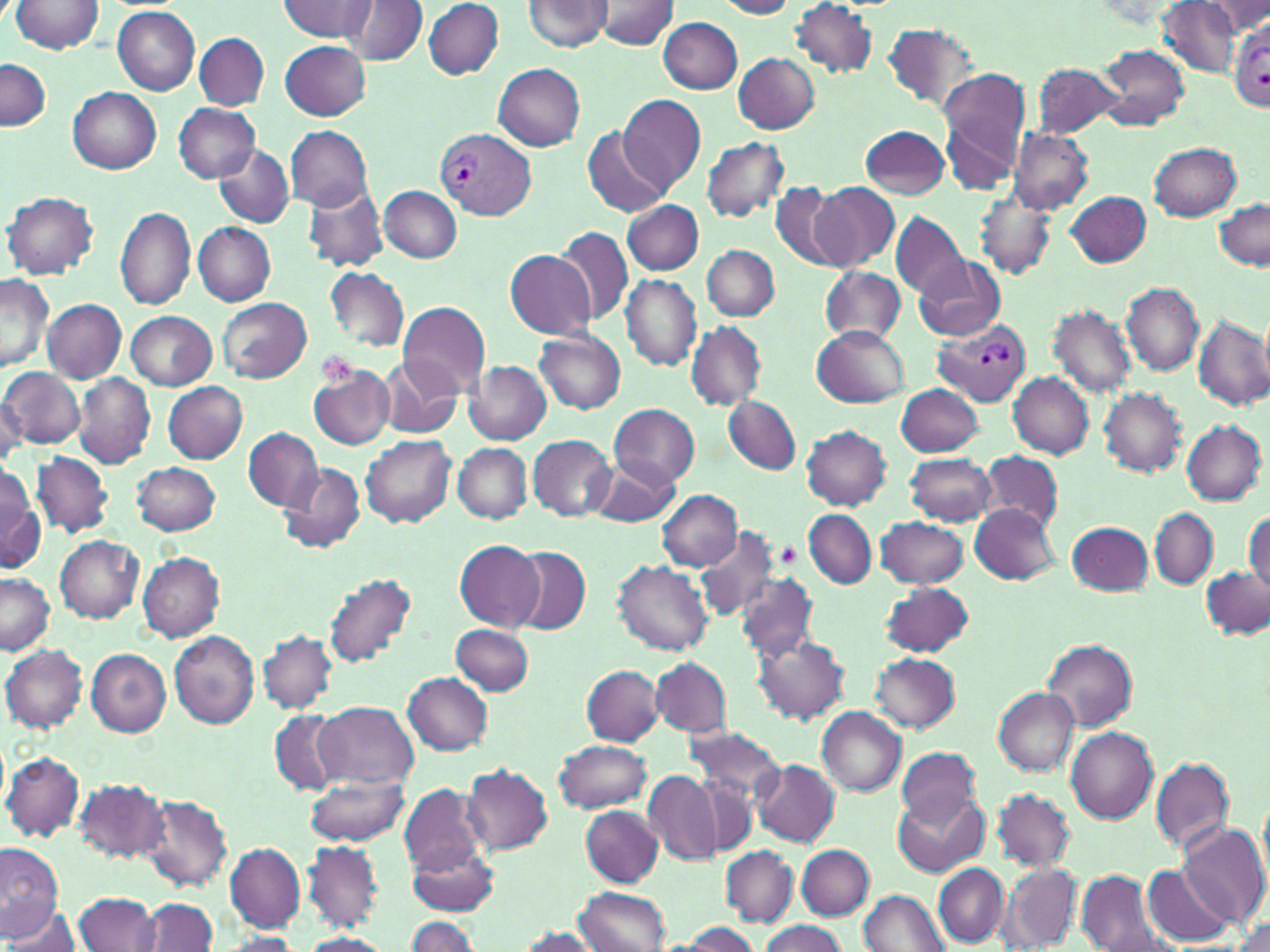
slide-level diagnosis = Plasmodium vivax
modality = optical microscopy
Plasmodium vivax-infected red blood cell locations = approximate bounding boxes as (x1, y1, x2, y2) in pixels: (1230, 21, 1270, 112), (437, 129, 534, 218), (933, 321, 1032, 406)
platelet locations = approximate bounding boxes as (x1, y1, x2, y2) in pixels: (314, 350, 360, 388), (778, 545, 800, 569)
preparation = thin blood smear
field of view = one of a larger specimen
uninfected red blood cell locations = approximate bounding boxes as (x1, y1, x2, y2) in pixels: (10, 0, 104, 55), (280, 0, 377, 43), (524, 0, 611, 52), (594, 0, 680, 49), (714, 0, 799, 18), (347, 1, 426, 66), (423, 1, 503, 79), (1207, 1, 1268, 36), (790, 2, 878, 77), (1158, 2, 1241, 77), (111, 6, 200, 95), (659, 17, 743, 94), (882, 22, 979, 112), (195, 32, 269, 110), (280, 41, 371, 120), (1095, 43, 1190, 131), (734, 53, 820, 133), (1, 59, 50, 131), (1033, 62, 1125, 139), (492, 63, 585, 150), (935, 67, 1031, 190), (69, 88, 161, 174), (618, 94, 706, 194), (174, 102, 259, 182), (286, 125, 373, 212), (860, 125, 949, 199), (583, 126, 671, 218), (1007, 128, 1092, 213), (702, 137, 788, 221), (214, 143, 294, 228), (1149, 143, 1242, 221), (769, 180, 852, 272), (809, 183, 899, 271), (302, 185, 389, 273), (379, 185, 461, 263), (976, 190, 1055, 280), (3, 191, 98, 279), (1067, 191, 1152, 267), (623, 200, 703, 275), (1214, 200, 1269, 270), (115, 205, 197, 311), (891, 213, 969, 300), (193, 223, 276, 305), (557, 227, 634, 325), (702, 245, 778, 320), (504, 248, 595, 340), (911, 254, 1005, 341), (819, 265, 907, 347), (326, 267, 409, 352), (0, 273, 54, 373), (620, 274, 702, 372), (1122, 283, 1205, 375), (217, 297, 311, 382), (43, 298, 126, 383), (397, 301, 491, 397), (1047, 304, 1135, 399), (126, 312, 215, 389), (1193, 314, 1270, 410), (685, 323, 766, 410), (811, 325, 908, 408), (535, 331, 625, 414), (382, 358, 462, 439), (461, 360, 551, 444), (308, 365, 395, 451), (1, 368, 85, 448), (1009, 372, 1094, 458), (74, 374, 156, 469), (163, 382, 247, 463), (897, 384, 986, 456), (1099, 386, 1187, 476), (0, 391, 26, 465), (725, 396, 800, 474), (611, 404, 699, 486), (1182, 421, 1266, 505), (802, 425, 891, 509), (242, 429, 322, 511), (362, 434, 455, 527), (527, 435, 618, 521), (453, 444, 531, 523), (31, 451, 114, 538), (980, 451, 1064, 529), (905, 453, 996, 525), (591, 455, 680, 527), (133, 461, 221, 535), (277, 462, 366, 556), (0, 472, 43, 576), (657, 489, 742, 570), (969, 504, 1061, 584), (1151, 508, 1217, 589), (803, 510, 876, 588), (1246, 511, 1269, 596), (876, 516, 968, 588), (1069, 521, 1153, 595), (694, 526, 786, 621), (55, 535, 144, 622), (453, 539, 544, 631), (510, 547, 591, 634), (138, 553, 225, 641), (614, 560, 713, 655), (1202, 567, 1268, 638), (735, 571, 819, 660), (324, 572, 417, 668), (0, 573, 54, 655), (880, 582, 975, 657), (451, 625, 534, 696), (168, 630, 259, 730), (259, 630, 337, 714), (751, 633, 853, 725), (1041, 639, 1136, 732), (1, 644, 88, 732), (86, 648, 172, 736), (870, 653, 959, 732), (651, 657, 731, 738), (582, 665, 663, 746), (403, 672, 493, 753), (993, 688, 1079, 775), (315, 701, 418, 788), (818, 707, 906, 797), (269, 711, 340, 793), (687, 725, 788, 812), (1066, 726, 1159, 822), (554, 739, 652, 813), (897, 747, 981, 826), (2, 750, 84, 842), (1152, 757, 1234, 856), (751, 759, 840, 848), (462, 763, 553, 855), (644, 771, 720, 864), (305, 775, 409, 846), (73, 778, 168, 863), (399, 785, 487, 879), (993, 788, 1074, 871), (894, 792, 988, 878), (139, 794, 232, 891), (582, 806, 663, 886), (1176, 823, 1269, 930), (303, 841, 382, 930), (0, 842, 64, 938), (224, 843, 305, 932), (408, 844, 500, 915), (797, 844, 874, 920), (721, 846, 797, 926), (998, 864, 1082, 951), (933, 865, 1009, 945), (1142, 865, 1234, 947), (1074, 870, 1173, 952), (575, 888, 670, 952), (859, 890, 950, 952), (75, 892, 161, 952), (138, 898, 217, 951), (5, 905, 86, 951), (405, 916, 479, 952), (1232, 916, 1270, 952), (674, 921, 760, 951), (759, 921, 847, 952), (515, 927, 604, 951), (218, 933, 302, 951), (297, 933, 394, 952)
magnification = 1000x
image size = 1270×952 pixels
stain = May-Grünwald-Giemsa